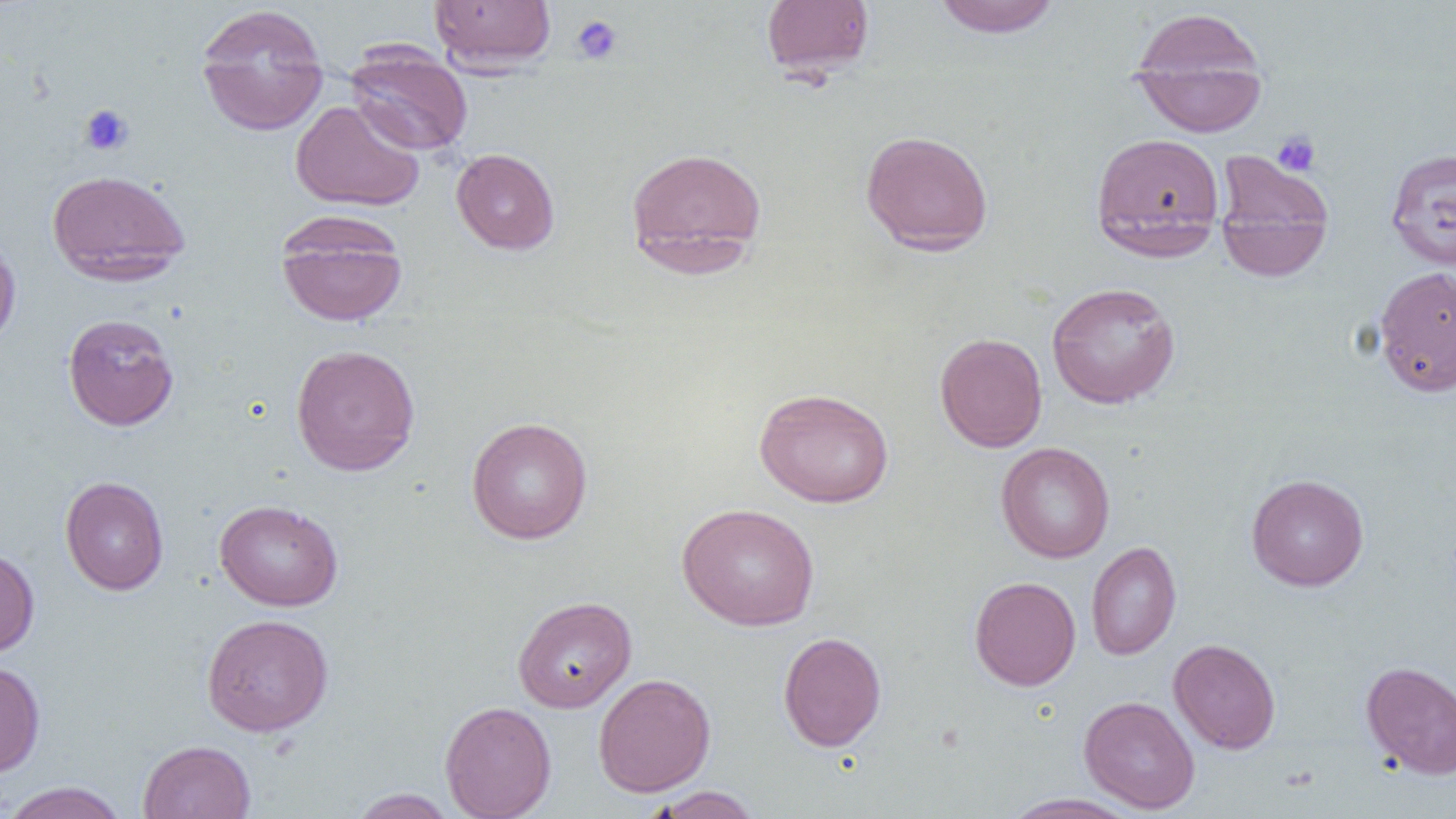 Approximate bounding boxes as named x1/y1/x2/y2 corners in pixels. Uninfected red blood cell locations: (x1=429, y1=0, x2=555, y2=72), (x1=760, y1=0, x2=875, y2=80), (x1=932, y1=0, x2=1061, y2=38), (x1=195, y1=3, x2=329, y2=136), (x1=1128, y1=10, x2=1267, y2=137), (x1=345, y1=44, x2=473, y2=156), (x1=290, y1=99, x2=425, y2=212), (x1=860, y1=130, x2=994, y2=255), (x1=1090, y1=131, x2=1225, y2=259), (x1=624, y1=145, x2=768, y2=272), (x1=451, y1=148, x2=560, y2=254), (x1=1385, y1=148, x2=1456, y2=270), (x1=1214, y1=150, x2=1334, y2=279), (x1=47, y1=169, x2=191, y2=285), (x1=275, y1=211, x2=408, y2=328), (x1=0, y1=236, x2=21, y2=349), (x1=1373, y1=265, x2=1456, y2=397), (x1=1046, y1=281, x2=1181, y2=409), (x1=62, y1=313, x2=179, y2=431), (x1=934, y1=332, x2=1048, y2=452), (x1=290, y1=343, x2=421, y2=476), (x1=754, y1=387, x2=894, y2=508), (x1=466, y1=416, x2=594, y2=544), (x1=995, y1=442, x2=1115, y2=563), (x1=1246, y1=474, x2=1369, y2=591), (x1=60, y1=476, x2=169, y2=595), (x1=214, y1=499, x2=343, y2=611), (x1=677, y1=503, x2=820, y2=631), (x1=1086, y1=541, x2=1182, y2=660), (x1=0, y1=546, x2=39, y2=658), (x1=969, y1=576, x2=1081, y2=691), (x1=512, y1=595, x2=637, y2=713), (x1=201, y1=613, x2=334, y2=736), (x1=778, y1=631, x2=886, y2=751), (x1=1168, y1=638, x2=1281, y2=754), (x1=1361, y1=660, x2=1456, y2=779), (x1=0, y1=661, x2=46, y2=777), (x1=592, y1=673, x2=716, y2=797), (x1=1079, y1=695, x2=1200, y2=813), (x1=440, y1=700, x2=557, y2=819), (x1=138, y1=740, x2=256, y2=819), (x1=0, y1=781, x2=130, y2=819), (x1=645, y1=786, x2=763, y2=819), (x1=348, y1=788, x2=457, y2=818), (x1=999, y1=792, x2=1145, y2=819). Platelet locations: (x1=571, y1=15, x2=624, y2=65), (x1=78, y1=104, x2=135, y2=156), (x1=1272, y1=131, x2=1320, y2=177). Slide-level diagnosis: no evidence of blood parasites. Captured at 1000x magnification. Optical microscopy. Image is 1456×819 pixels. Thin blood smear. Single field of view.